Locate every malaria parasite.
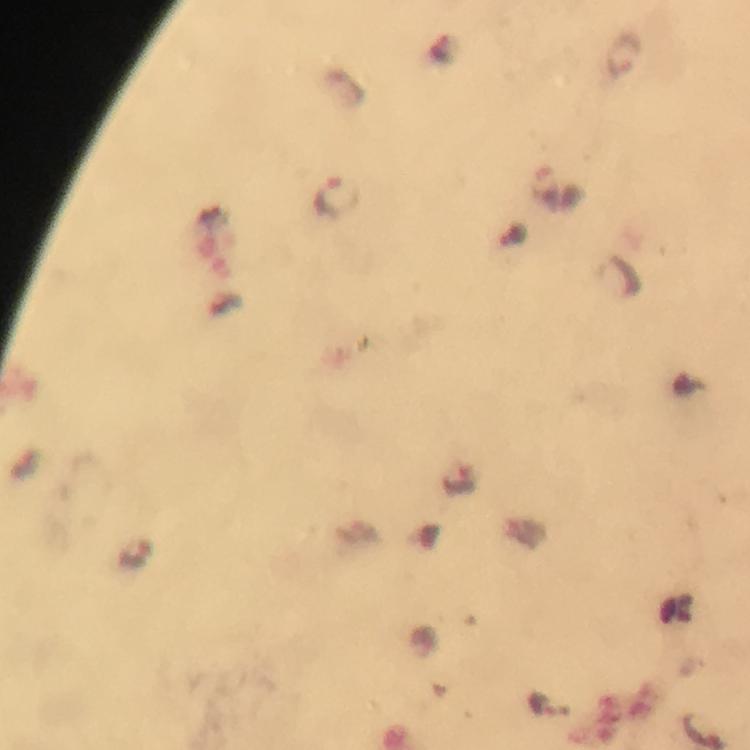

Approximate centers as [x, y] in pixels.
Malaria parasites: [623, 54], [338, 198], [461, 480].

From a diagnostic examination for malaria. Giemsa stain. Image is 750×750 pixels. Immersion oil applied. A crop from one field of view. Photographed through the microscope with a smartphone camera. At 100x magnification. Thick smear.